Name the parasite shown.
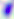
This is Toxoplasma gondii.

modality = micrograph
magnification = 400x